State which parasite is depicted.
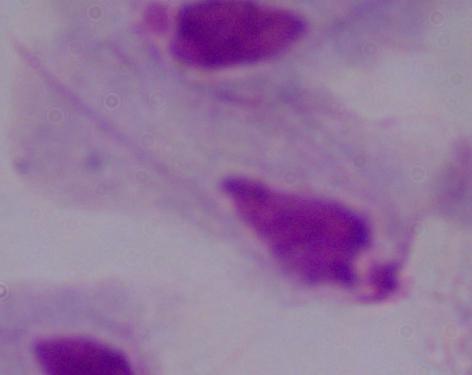
This is a trichomonad.

modality: photomicrograph
magnification: 1000x